Draw a bounding box around every parasitised red blood cell, every trophozoite, every gametocyte, every leukocyte, and every artifact (platelet-like body, stain precipitate, or debris).
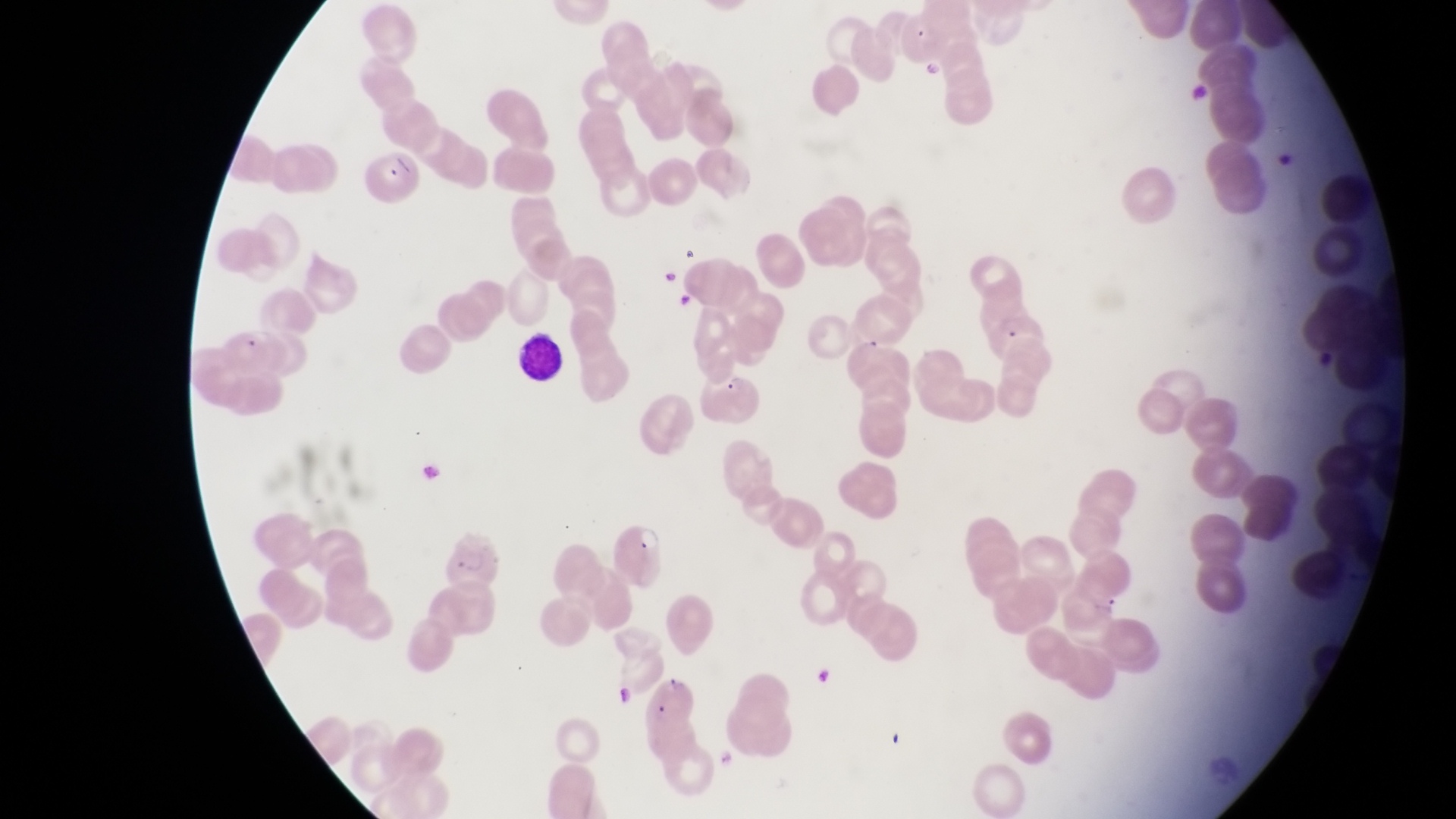
Approximate bounding boxes as [left, top, right, bottom] in pixels.
Parasitised red blood cells: [899, 10, 954, 68], [364, 148, 423, 211], [980, 303, 1041, 352], [701, 372, 760, 424], [610, 512, 671, 585], [655, 667, 702, 720].
Leukocytes: [515, 328, 565, 384].

field of view = single
capture = smartphone photograph through the eyepiece of an Olympus CX-23 microscope
preparation = thin blood film
country = Uganda
magnification = 1000x
image size = 1456×819 pixels